Comment on the morphology of the red blood cells.
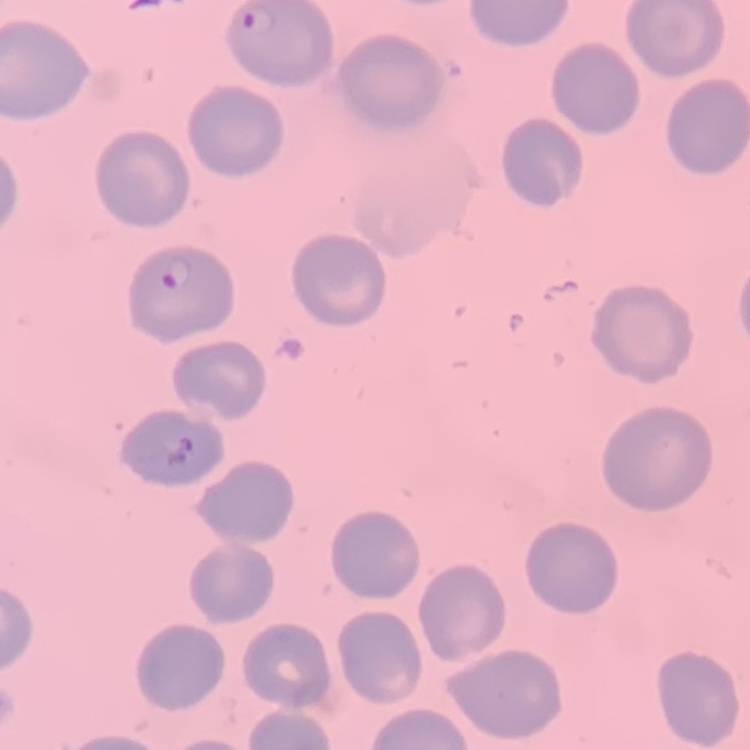
No rouleaux formation.

Summary:
  - Preparation: thin blood smear
  - Image type: square crop of a larger photomicrograph
  - Stain: Field's or Giemsa